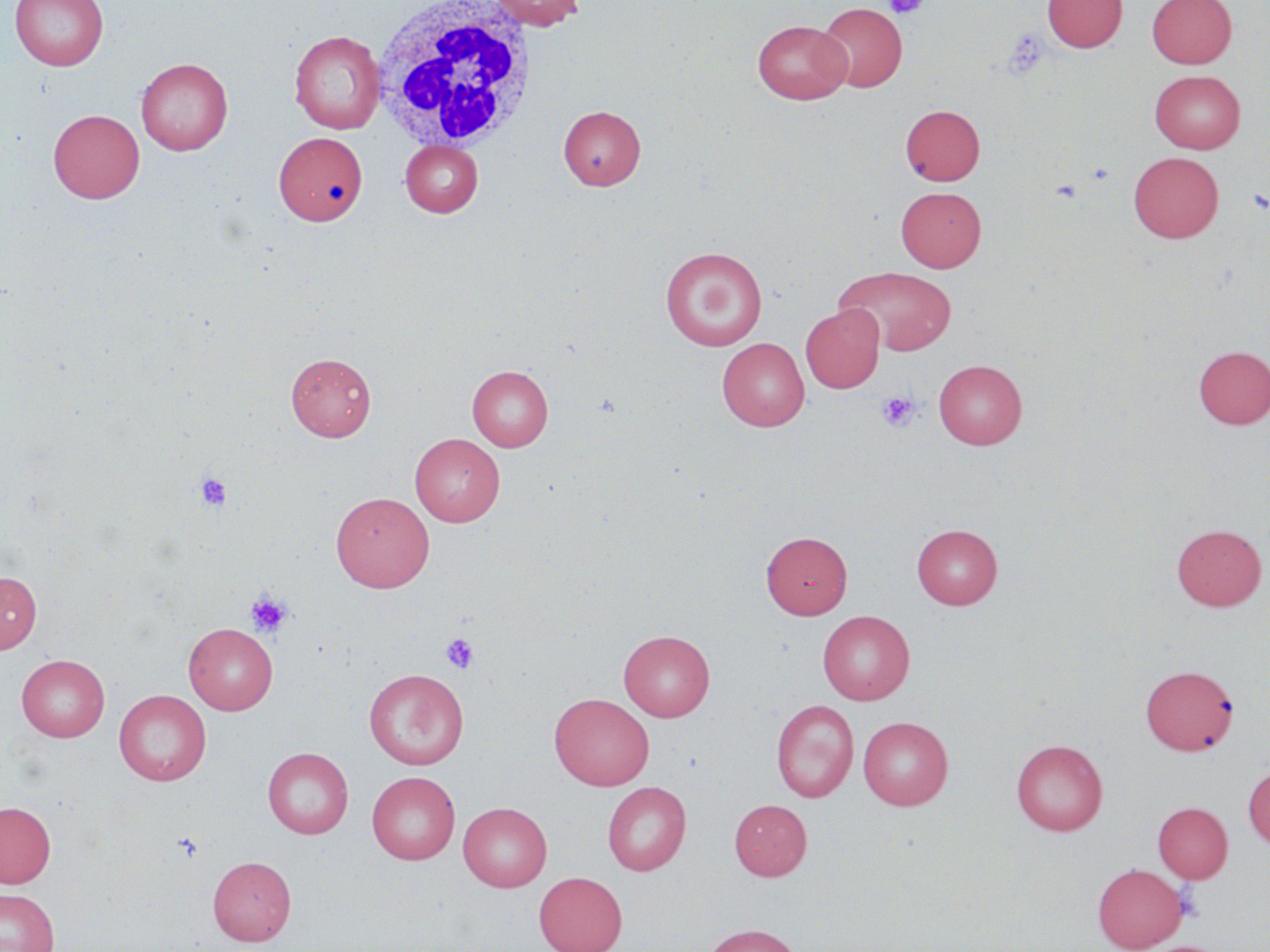

Summary:
  - Coordinate format: approximate bounding boxes as (x1, y1, x2, y2) in pixels
  - Platelet locations: (885, 0, 928, 19), (1004, 29, 1049, 79), (1248, 188, 1269, 215), (876, 391, 919, 432), (195, 472, 232, 511), (245, 591, 293, 638), (441, 633, 479, 673), (173, 833, 204, 862)
  - White blood cell locations: (370, 1, 540, 153)
  - Uninfected red blood cell locations: (10, 0, 108, 71), (485, 0, 587, 30), (1042, 0, 1127, 52), (1147, 0, 1237, 68), (816, 3, 907, 92), (752, 19, 851, 104), (289, 30, 385, 133), (136, 58, 233, 155), (1150, 70, 1245, 153), (900, 104, 985, 185), (558, 105, 645, 190), (48, 109, 144, 203), (274, 131, 367, 226), (400, 140, 483, 217), (1129, 152, 1223, 243), (895, 186, 986, 272), (660, 246, 767, 350), (835, 266, 957, 356), (800, 305, 884, 392), (717, 338, 809, 431), (1193, 345, 1270, 428), (286, 352, 376, 441), (933, 359, 1027, 448), (467, 365, 553, 451), (410, 433, 505, 526), (331, 492, 435, 591), (912, 523, 1002, 609), (1171, 524, 1267, 611), (761, 531, 852, 619), (0, 572, 41, 654), (818, 610, 914, 704), (183, 623, 277, 715), (618, 630, 715, 721), (16, 653, 110, 741), (1140, 665, 1237, 755), (363, 668, 468, 769), (114, 690, 211, 786), (549, 693, 654, 790), (771, 699, 858, 802), (858, 716, 953, 809), (1011, 739, 1108, 836), (262, 747, 353, 838), (1243, 765, 1270, 849), (366, 771, 460, 864), (602, 782, 691, 876), (729, 799, 812, 880), (0, 802, 56, 888), (458, 802, 552, 891), (1153, 802, 1233, 883), (207, 856, 296, 945), (1092, 863, 1188, 951), (534, 871, 627, 952), (0, 888, 60, 952), (702, 923, 803, 952)
  - Slide-level diagnosis: no evidence of blood parasites
  - Image size: 1270×952 pixels
  - Magnification: 1000x
  - Preparation: thin blood film
  - Field of view: one of a larger specimen
  - Stain: May-Grünwald-Giemsa
  - Modality: light microscopy